Classify this cell by malaria status.
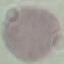

It is uninfected.

Photographed with a smartphone camera at the microscope eyepiece. Giemsa stain. Cell patch, automatically extracted from a larger field of view and resized to 64 × 64 pixels. Thin smear of blood.